Identify the blood parasite species.
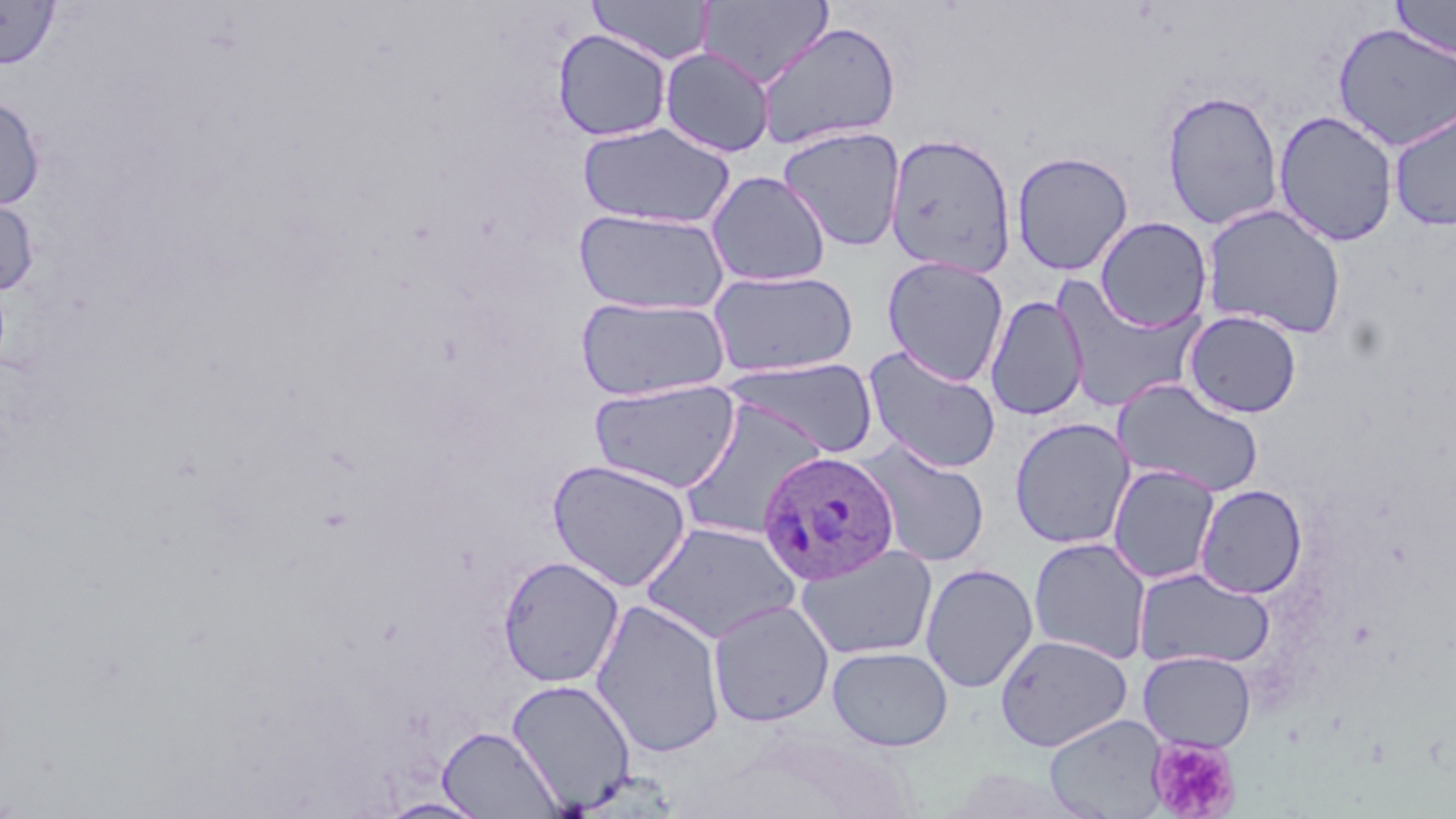

Plasmodium ovale.

modality = optical microscopy
uninfected red blood cell locations = approximate bounding boxes as [x1, y1, x2, y2] in pixels: [1390, 0, 1456, 60], [0, 1, 60, 69], [586, 1, 714, 65], [696, 1, 834, 89], [754, 21, 902, 150], [1332, 23, 1456, 152], [552, 28, 672, 142], [659, 47, 775, 157], [1160, 89, 1284, 230], [0, 96, 45, 211], [1388, 106, 1456, 230], [1273, 110, 1399, 246], [577, 121, 736, 229], [777, 126, 906, 251], [884, 132, 1017, 277], [1011, 151, 1133, 276], [706, 170, 831, 287], [0, 194, 39, 298], [1199, 203, 1347, 339], [573, 208, 731, 316], [1095, 216, 1212, 332], [882, 255, 1009, 386], [707, 269, 859, 378], [1052, 275, 1206, 413], [575, 295, 731, 402], [986, 295, 1089, 421], [1184, 310, 1303, 419], [862, 345, 1002, 474], [722, 358, 879, 458], [1113, 377, 1264, 498], [588, 379, 742, 493], [678, 396, 829, 541], [1009, 416, 1135, 550], [857, 439, 991, 567], [547, 458, 693, 592], [1107, 463, 1221, 585], [1195, 484, 1308, 599], [640, 520, 802, 645], [1029, 537, 1152, 664], [795, 544, 938, 661], [497, 555, 624, 688], [921, 563, 1039, 693], [1134, 567, 1275, 670], [590, 598, 726, 757], [708, 599, 834, 727], [995, 634, 1132, 751], [828, 645, 953, 751], [1138, 651, 1256, 752], [507, 678, 636, 811], [1044, 714, 1169, 819], [437, 725, 563, 818], [376, 796, 492, 818]
Plasmodium ovale-infected red blood cell locations = approximate bounding boxes as [x1, y1, x2, y2] in pixels: [757, 450, 901, 585]
platelet locations = approximate bounding boxes as [x1, y1, x2, y2] in pixels: [1147, 737, 1241, 818]
image size = 1456×819 pixels
preparation = thin blood film
stain = May-Grünwald-Giemsa
magnification = 1000x
field of view = one of a larger specimen